Name the parasite shown.
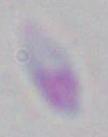
This is Toxoplasma gondii.

Micrograph. 1000x magnification.